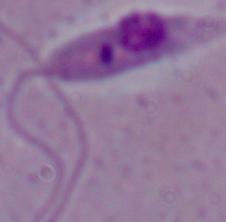
magnification: 1000x
modality: photomicrograph
identification: Leishmania